Report the malaria status of this cell.
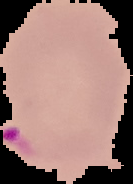
Parasitized.

Summary:
  - Preparation: thin blood film
  - Image size: 133×184 pixels
  - Image type: segmented cell region with the area outside set to black